Name the parasite shown.
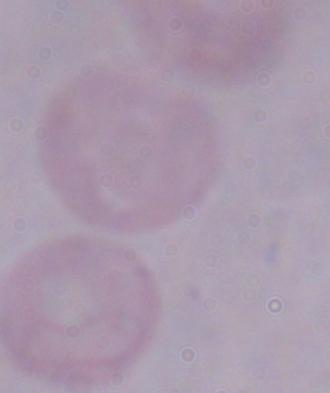
A trypanosome.

magnification = 1000x
modality = micrograph